Assess for Plasmodium parasites.
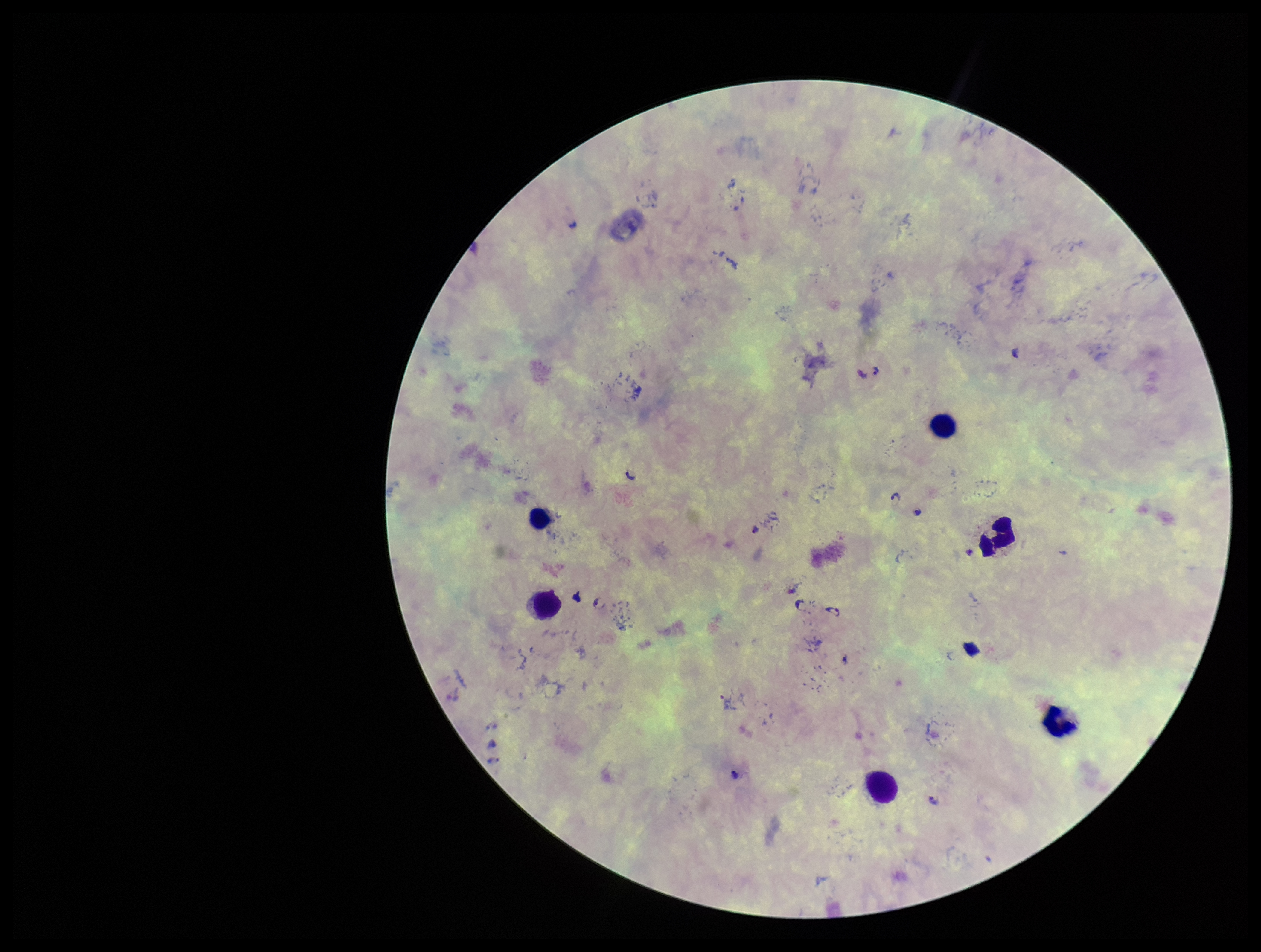
Detected.

Single field of view. Patient malaria status: positive. Leukocyte count: 6. Parasite count: 7. Stained with Giemsa. Species reported for this patient: Plasmodium falciparum. Preparation: thick. Image is 1261×952 pixels. Photographed through the microscope eyepiece with a smartphone camera.